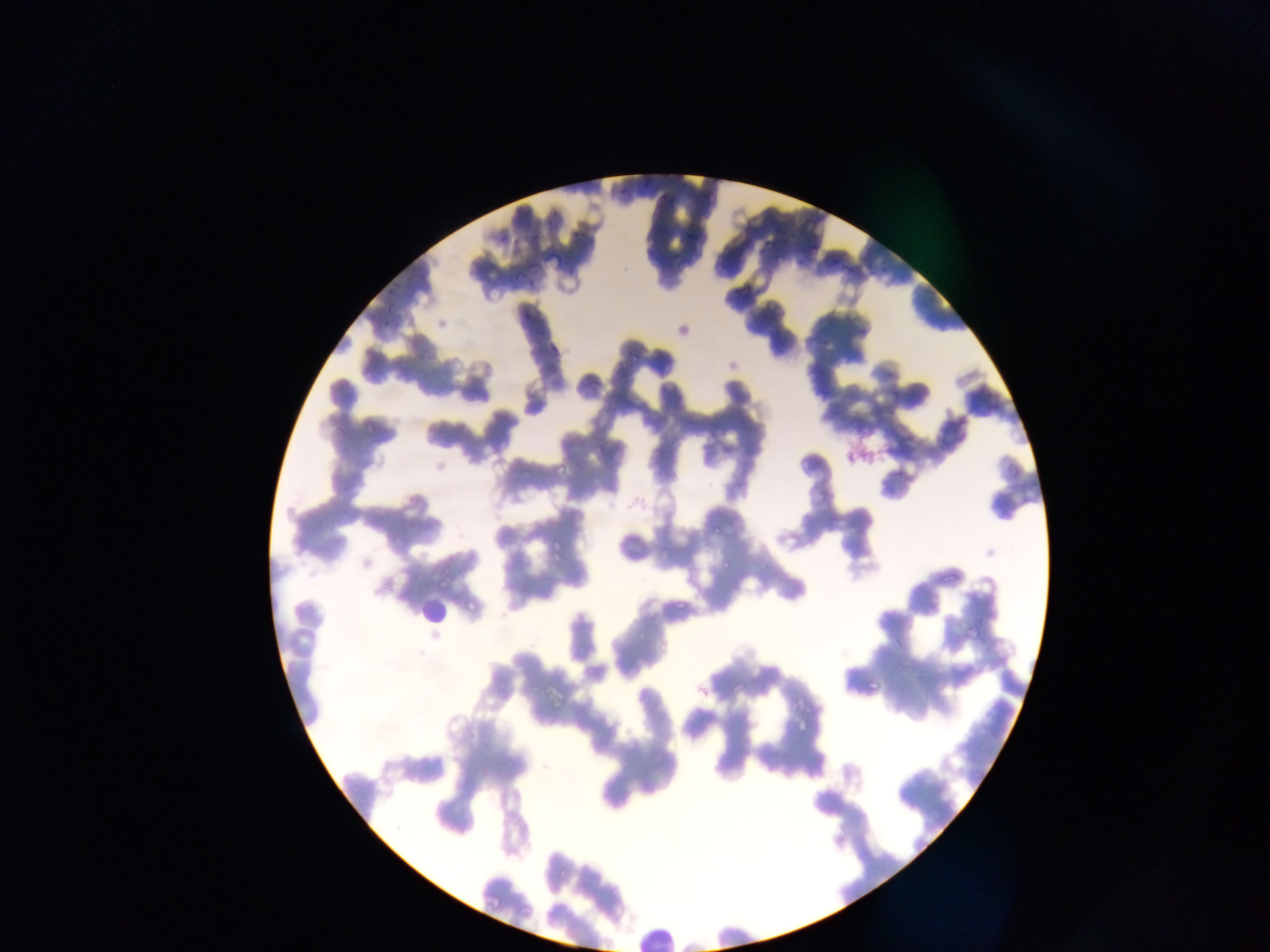 Approximate bounding boxes as left top right bottom in pixels. Leukocyte locations: 423 594 446 626; 636 922 682 952. Malaria parasite locations: 627 349 644 367; 449 353 475 372; 480 438 497 459; 555 458 567 477; 708 517 732 535; 547 537 561 558; 715 557 736 568; 438 576 460 586; 670 588 688 610; 459 596 474 612; 961 624 983 641; 869 673 881 692; 545 675 568 704; 795 714 810 732; 517 901 534 915. Single field of view. Image is 1270×952 pixels. Thin blood smear. Photographed through a microscope with a mobile-phone camera. Collected in Ghana.